Identify the parasite.
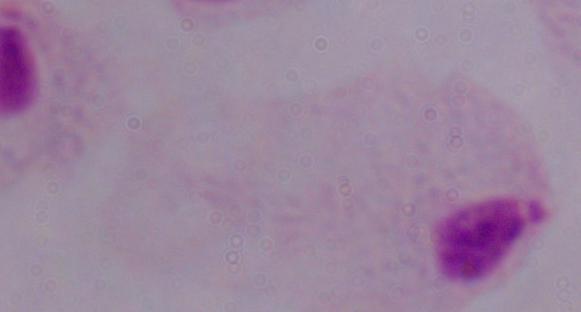
A trichomonad.

Summary:
  - Modality: micrograph
  - Magnification: 1000x